Give the position of every leukocyte visible.
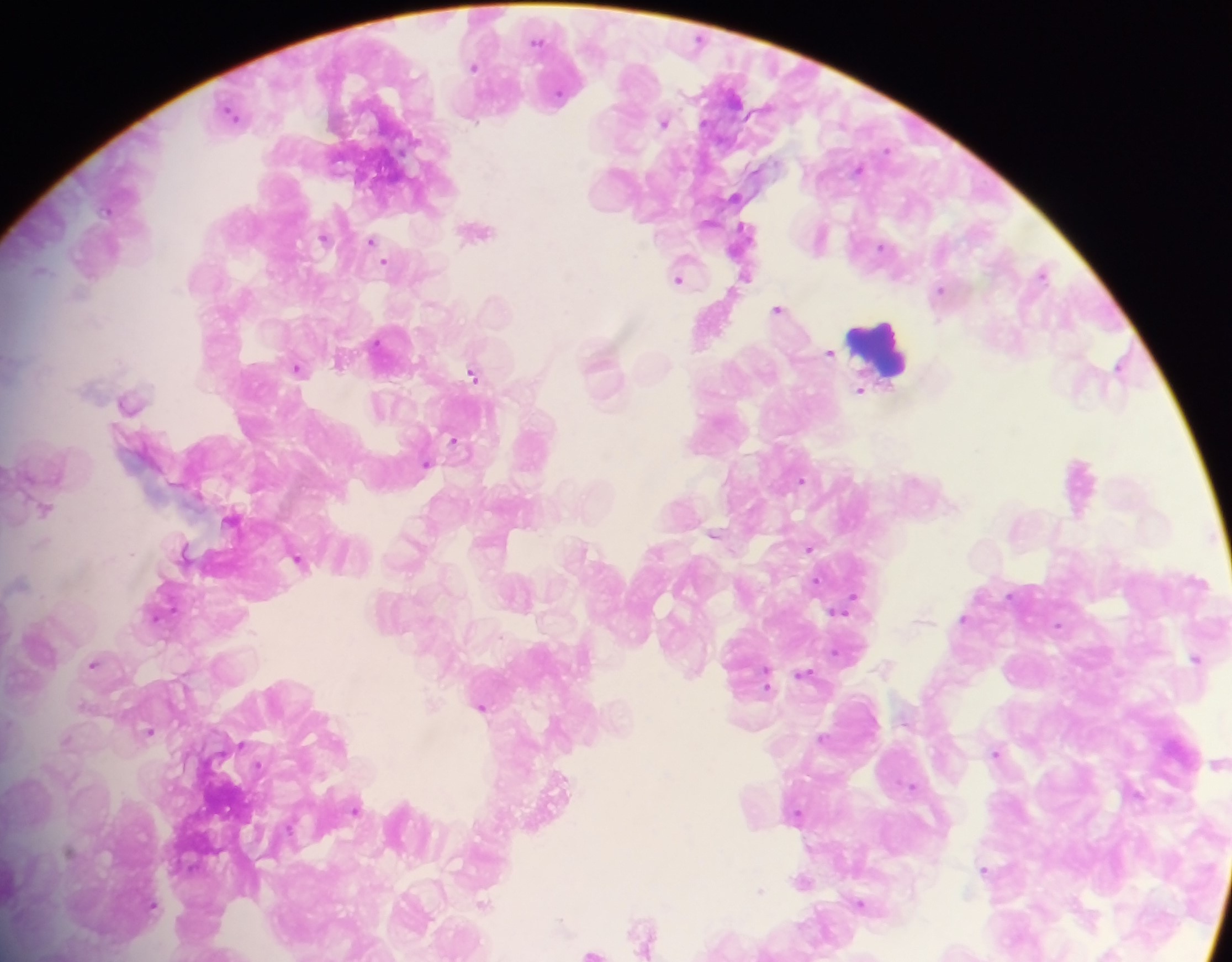

Approximate centers as [x, y] in pixels.
Leukocytes: [878, 347].

Malaria parasite locations: [537, 41], [473, 66], [232, 113], [664, 123], [887, 150], [859, 169], [478, 230], [323, 238], [371, 241], [883, 247], [385, 262], [41, 271], [1042, 272], [746, 276], [678, 280], [940, 290], [777, 309], [378, 343], [829, 354], [339, 363], [1120, 365], [298, 368], [472, 374], [860, 390], [129, 403], [455, 441], [425, 465], [801, 480], [45, 509], [231, 519], [713, 535], [585, 548], [809, 548], [184, 550], [298, 560], [816, 581], [19, 582], [1009, 595], [853, 598], [839, 610], [156, 616], [963, 619], [1058, 625], [835, 653], [1196, 659], [94, 664], [694, 672], [766, 674], [805, 674], [766, 683], [85, 705], [431, 706], [482, 707], [149, 731], [823, 738], [67, 739], [996, 753], [1217, 764], [912, 786], [356, 810], [797, 814], [69, 852], [984, 870], [801, 882], [760, 891], [860, 903], [484, 904], [152, 905], [644, 934], [592, 952]. Mobile-phone photograph taken through the microscope. Thick blood smear. Image is 1232×962 pixels. One field of view. Collected in Ghana.